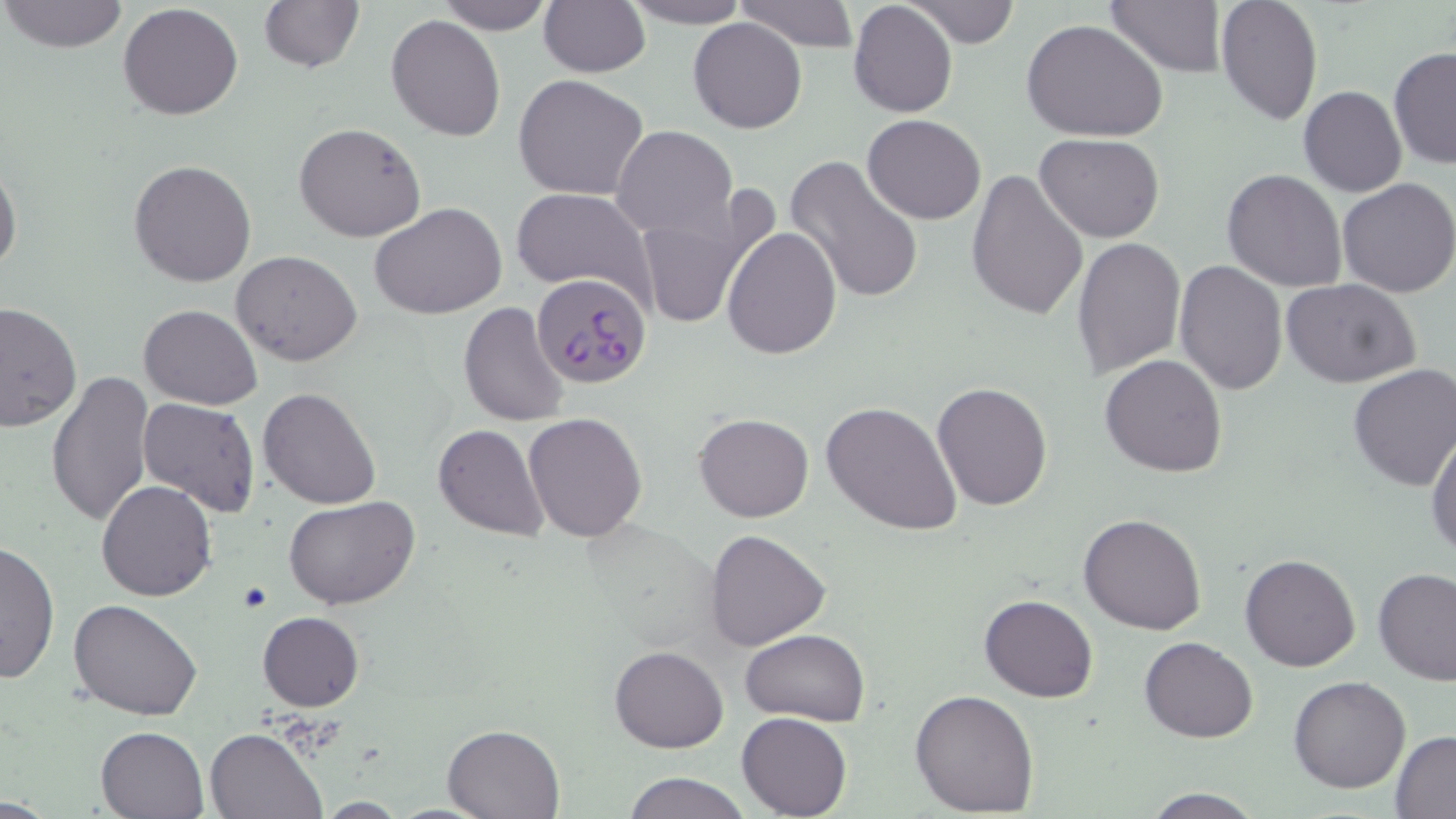

{
  "slide_level_diagnosis": "Plasmodium falciparum",
  "image_size": "1456×819 pixels",
  "stain": "May-Grünwald-Giemsa",
  "modality": "light microscopy",
  "magnification": "1000x",
  "preparation": "thin blood smear",
  "field_of_view": "single",
  "uninfected_red_blood_cell_locations": "approximate bounding boxes as named x1/y1/x2/y2 corners in pixels: (x1=1, y1=0, x2=128, y2=53), (x1=259, y1=0, x2=364, y2=73), (x1=435, y1=0, x2=554, y2=35), (x1=616, y1=0, x2=753, y2=28), (x1=731, y1=0, x2=860, y2=50), (x1=907, y1=0, x2=1019, y2=47), (x1=1104, y1=0, x2=1227, y2=76), (x1=1215, y1=0, x2=1321, y2=124), (x1=539, y1=1, x2=650, y2=77), (x1=849, y1=2, x2=958, y2=117), (x1=117, y1=3, x2=244, y2=120), (x1=386, y1=15, x2=507, y2=141), (x1=688, y1=18, x2=809, y2=133), (x1=1022, y1=19, x2=1169, y2=143), (x1=1389, y1=47, x2=1456, y2=168), (x1=514, y1=75, x2=649, y2=201), (x1=1298, y1=86, x2=1406, y2=197), (x1=862, y1=114, x2=986, y2=224), (x1=294, y1=122, x2=426, y2=243), (x1=613, y1=126, x2=737, y2=239), (x1=1036, y1=133, x2=1165, y2=241), (x1=786, y1=155, x2=925, y2=304), (x1=0, y1=157, x2=22, y2=279), (x1=129, y1=158, x2=257, y2=287), (x1=966, y1=169, x2=1088, y2=320), (x1=1222, y1=169, x2=1348, y2=293), (x1=1336, y1=177, x2=1456, y2=298), (x1=510, y1=186, x2=655, y2=298), (x1=634, y1=194, x2=775, y2=332), (x1=370, y1=201, x2=507, y2=319), (x1=722, y1=226, x2=842, y2=360), (x1=1071, y1=235, x2=1186, y2=381), (x1=232, y1=250, x2=363, y2=366), (x1=1175, y1=260, x2=1288, y2=394), (x1=1283, y1=277, x2=1422, y2=388), (x1=460, y1=301, x2=573, y2=427), (x1=0, y1=302, x2=81, y2=431), (x1=139, y1=304, x2=263, y2=411), (x1=1100, y1=354, x2=1228, y2=477), (x1=1347, y1=363, x2=1456, y2=491), (x1=47, y1=370, x2=154, y2=529), (x1=931, y1=382, x2=1053, y2=511), (x1=259, y1=387, x2=382, y2=511), (x1=138, y1=397, x2=261, y2=518), (x1=822, y1=399, x2=964, y2=537), (x1=523, y1=411, x2=649, y2=543), (x1=694, y1=412, x2=814, y2=522), (x1=432, y1=423, x2=548, y2=541), (x1=1426, y1=430, x2=1456, y2=558), (x1=96, y1=481, x2=218, y2=601), (x1=285, y1=495, x2=419, y2=608), (x1=1079, y1=512, x2=1207, y2=635), (x1=704, y1=529, x2=831, y2=651), (x1=0, y1=540, x2=59, y2=685), (x1=1240, y1=553, x2=1362, y2=671), (x1=1374, y1=567, x2=1456, y2=684), (x1=979, y1=594, x2=1098, y2=703), (x1=68, y1=597, x2=202, y2=721), (x1=257, y1=611, x2=365, y2=711), (x1=742, y1=629, x2=870, y2=726), (x1=1139, y1=637, x2=1257, y2=742), (x1=610, y1=644, x2=729, y2=751), (x1=1288, y1=676, x2=1411, y2=793), (x1=910, y1=687, x2=1040, y2=814), (x1=737, y1=711, x2=852, y2=818), (x1=442, y1=722, x2=567, y2=817), (x1=96, y1=725, x2=209, y2=818), (x1=204, y1=726, x2=326, y2=818), (x1=1390, y1=732, x2=1456, y2=816), (x1=621, y1=770, x2=751, y2=819), (x1=1141, y1=788, x2=1266, y2=819), (x1=311, y1=798, x2=408, y2=817)",
  "plasmodium_falciparum_infected_red_blood_cell_locations": "approximate bounding boxes as named x1/y1/x2/y2 corners in pixels: (x1=532, y1=273, x2=650, y2=387)"
}